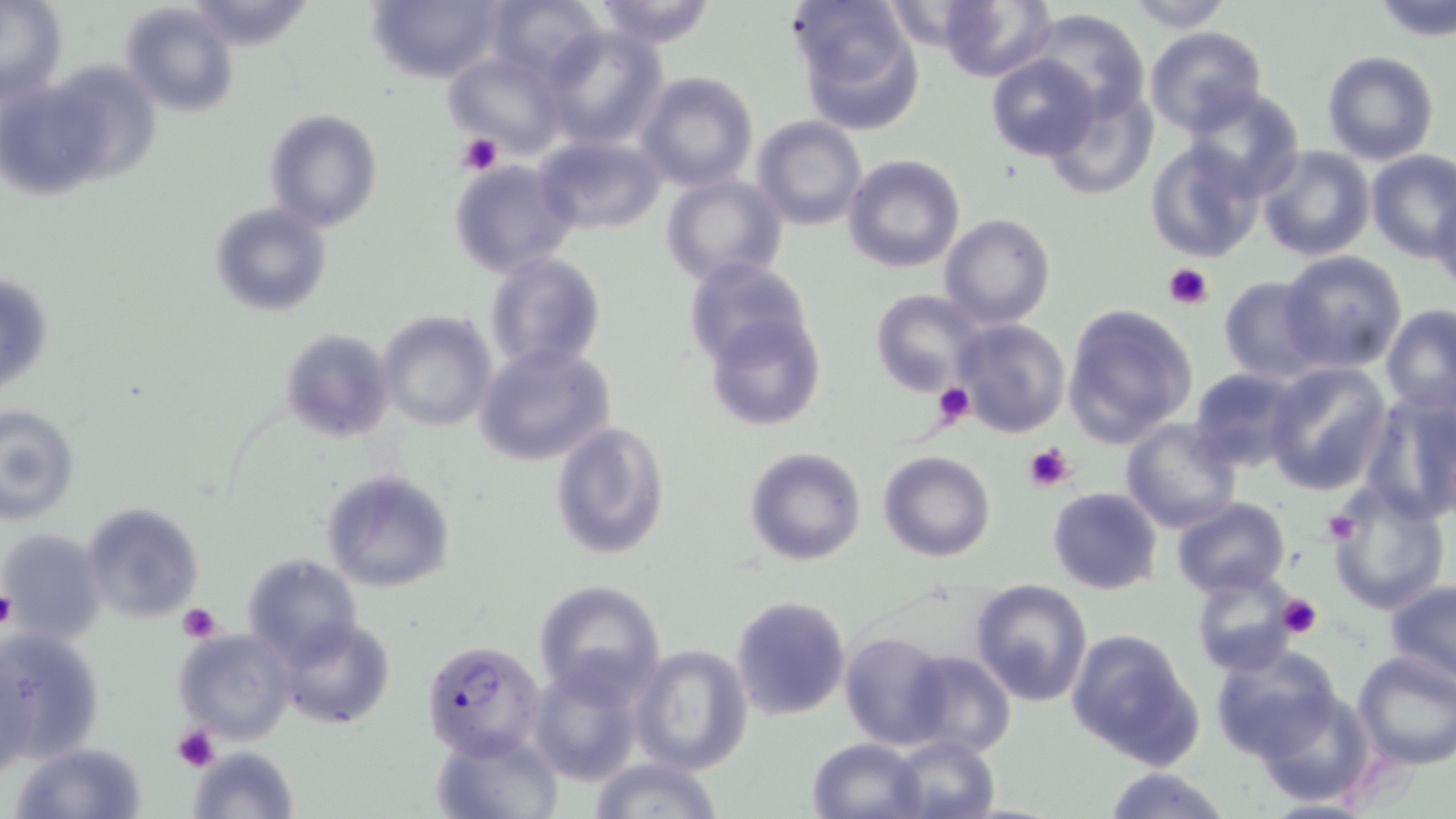
slide_level_diagnosis: Plasmodium falciparum
image_size: 1456×819 pixels
plasmodium_falciparum_infected_red_blood_cell_locations: 'approximate bounding boxes as [x1, y1, x2, y2] in pixels: [421, 637, 546, 759]'
preparation: thin blood smear
platelet_locations: 'approximate bounding boxes as [x1, y1, x2, y2] in pixels: [457, 132, 501, 175], [1163, 262, 1212, 309], [931, 382, 976, 430], [1022, 441, 1076, 492], [1323, 511, 1361, 545], [0, 586, 16, 631], [1275, 593, 1323, 640], [177, 603, 222, 644], [170, 725, 221, 773]'
stain: May-Grünwald-Giemsa
field_of_view: one of a larger specimen
magnification: 1000x
uninfected_red_blood_cell_locations: 'approximate bounding boxes as [x1, y1, x2, y2] in pixels: [365, 0, 505, 84], [484, 0, 605, 83], [591, 0, 718, 48], [787, 0, 925, 131], [937, 0, 1058, 83], [1122, 0, 1235, 31], [1372, 0, 1456, 44], [181, 1, 314, 48], [880, 1, 994, 53], [0, 2, 68, 100], [119, 3, 240, 118], [1021, 10, 1150, 123], [1143, 25, 1269, 136], [541, 26, 666, 149], [442, 50, 568, 159], [985, 52, 1105, 160], [1321, 52, 1438, 165], [64, 66, 157, 182], [635, 70, 760, 190], [4, 78, 99, 206], [1044, 86, 1157, 200], [1182, 86, 1305, 199], [262, 108, 383, 232], [752, 116, 867, 232], [536, 134, 667, 235], [1143, 139, 1264, 264], [1257, 146, 1375, 262], [1366, 150, 1456, 261], [843, 154, 967, 274], [448, 158, 582, 279], [660, 173, 787, 289], [1431, 188, 1456, 296], [208, 201, 333, 318], [939, 213, 1055, 329], [1278, 250, 1408, 372], [482, 252, 608, 376], [682, 258, 816, 374], [0, 271, 53, 395], [1219, 276, 1332, 382], [872, 289, 987, 396], [1061, 304, 1197, 446], [1381, 304, 1456, 416], [700, 306, 826, 434], [375, 309, 498, 432], [950, 318, 1072, 439], [280, 327, 395, 442], [473, 341, 617, 467], [1265, 363, 1392, 495], [1188, 366, 1304, 475], [1362, 390, 1456, 525], [1, 402, 79, 524], [1120, 417, 1243, 534], [548, 421, 670, 561], [744, 447, 866, 567], [879, 451, 996, 562], [320, 467, 454, 594], [1326, 481, 1450, 614], [1047, 487, 1163, 594], [1171, 497, 1290, 597], [80, 502, 205, 625], [0, 528, 106, 644], [241, 554, 363, 666], [1191, 569, 1296, 676], [970, 578, 1092, 706], [534, 579, 667, 701], [1385, 580, 1456, 688], [730, 595, 851, 721], [272, 614, 396, 730], [0, 626, 106, 768], [172, 628, 298, 746], [1065, 628, 1203, 771], [839, 632, 952, 747], [630, 644, 752, 777], [1210, 646, 1347, 763], [901, 649, 1015, 758], [1352, 649, 1456, 770], [528, 660, 645, 785], [1251, 686, 1377, 809], [431, 724, 563, 819], [889, 735, 999, 819], [808, 737, 926, 819], [10, 741, 150, 819], [185, 745, 299, 818], [586, 755, 726, 819], [1103, 767, 1233, 819]'
modality: optical microscopy